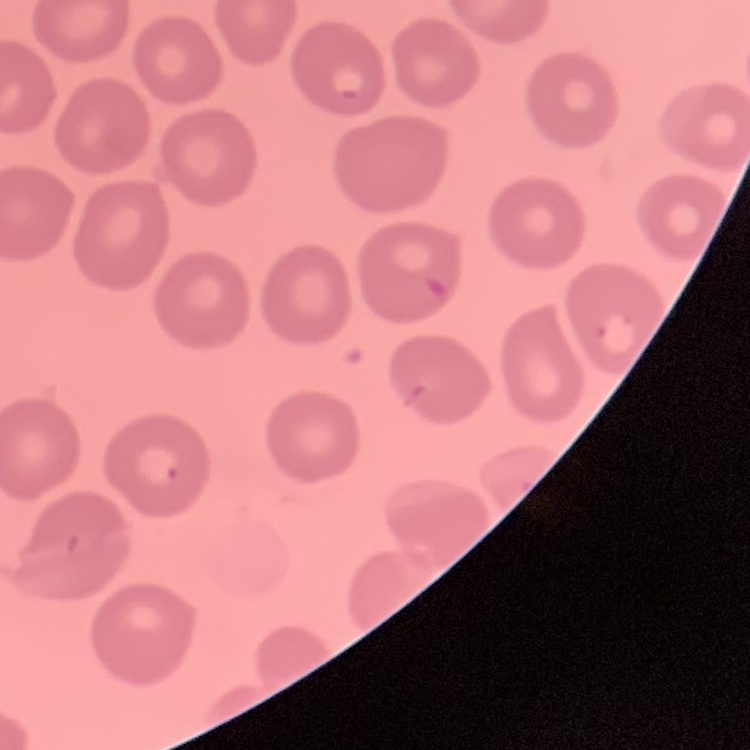
Summary:
  - Red blood cell morphology: no rouleaux formation
  - Preparation: thin blood film
  - Stain: Field's or Giemsa
  - Image type: one tile cut from a larger photomicrograph